Assess this cell for malaria.
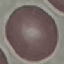
It is uninfected.

Summary:
  - Image type: automatically extracted cell patch, resized to 64 × 64 pixels
  - Stain: Giemsa
  - Capture: smartphone through the microscope eyepiece
  - Preparation: thin blood film